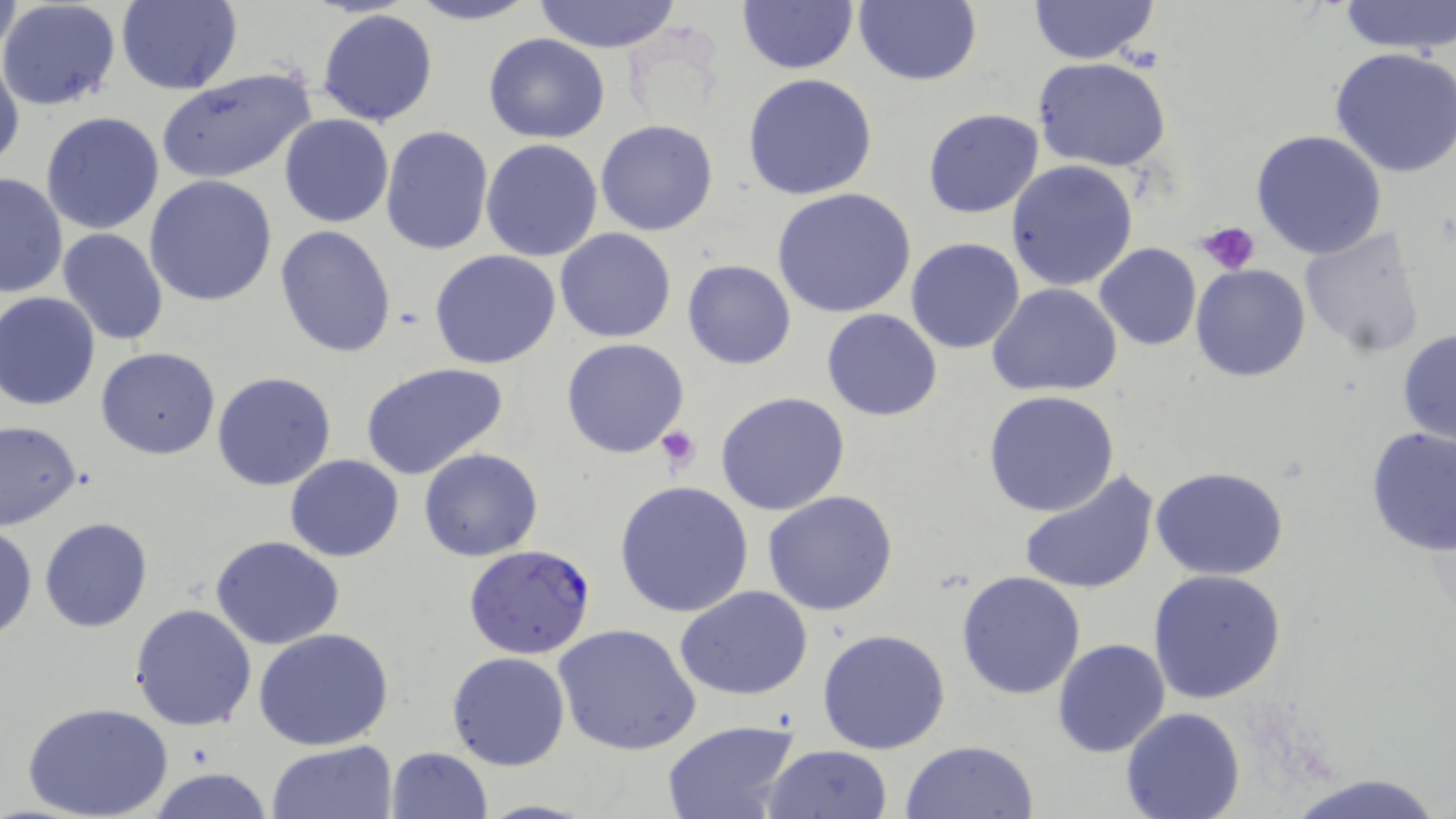

{
  "slide_level_diagnosis": "Plasmodium falciparum",
  "modality": "optical microscopy",
  "magnification": "1000x",
  "field_of_view": "single",
  "platelet_locations": "approximate bounding boxes as (x1, y1, x2, y2) in pixels: (1194, 222, 1261, 275), (657, 425, 700, 472)",
  "image_size": "1456×819 pixels",
  "preparation": "thin blood smear",
  "uninfected_red_blood_cell_locations": "approximate bounding boxes as (x1, y1, x2, y2) in pixels: (0, 0, 123, 110), (0, 0, 21, 68), (115, 0, 242, 95), (403, 0, 540, 26), (529, 0, 684, 52), (735, 0, 858, 74), (855, 0, 983, 87), (1029, 0, 1159, 65), (1337, 0, 1455, 55), (315, 9, 440, 127), (483, 33, 612, 144), (1328, 46, 1456, 177), (0, 51, 24, 177), (1033, 58, 1172, 170), (156, 67, 317, 185), (743, 73, 878, 201), (922, 108, 1045, 218), (41, 110, 165, 234), (279, 114, 394, 227), (595, 120, 720, 236), (380, 125, 494, 255), (1249, 130, 1389, 261), (480, 139, 603, 262), (1006, 161, 1138, 291), (0, 172, 66, 300), (144, 175, 277, 306), (772, 188, 918, 320), (275, 225, 397, 357), (1298, 225, 1427, 359), (58, 229, 170, 346), (554, 229, 677, 343), (905, 238, 1027, 355), (1094, 243, 1202, 351), (430, 248, 562, 369), (682, 259, 797, 370), (1190, 264, 1311, 382), (988, 283, 1123, 396), (1, 292, 101, 411), (822, 307, 943, 421), (1397, 328, 1456, 446), (561, 338, 690, 458), (96, 346, 220, 459), (361, 363, 512, 482), (212, 372, 338, 491), (983, 390, 1121, 518), (717, 391, 851, 516), (0, 420, 82, 530), (1363, 425, 1456, 557), (419, 449, 543, 562), (285, 454, 405, 561), (1150, 465, 1290, 581), (1019, 470, 1158, 595), (613, 480, 755, 618), (761, 490, 899, 615), (39, 517, 153, 633), (0, 524, 37, 641), (211, 535, 344, 649), (1147, 567, 1288, 704), (955, 570, 1087, 700), (676, 585, 813, 701), (129, 603, 258, 732), (555, 624, 702, 757), (817, 628, 951, 754), (254, 630, 394, 751), (1051, 639, 1171, 757), (445, 652, 570, 771), (24, 701, 174, 819), (1121, 708, 1246, 819), (660, 719, 801, 819), (266, 740, 398, 819), (899, 740, 1040, 819), (762, 744, 893, 819), (386, 747, 492, 819), (149, 767, 272, 818), (1284, 772, 1448, 819)",
  "stain": "May-Grünwald-Giemsa",
  "plasmodium_falciparum_infected_red_blood_cell_locations": "approximate bounding boxes as (x1, y1, x2, y2) in pixels: (463, 544, 596, 659)"
}